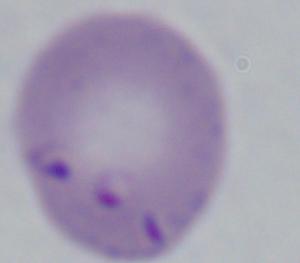

modality = micrograph
magnification = 1000x
identification = Babesia